Locate every blood parasite and identify its species.
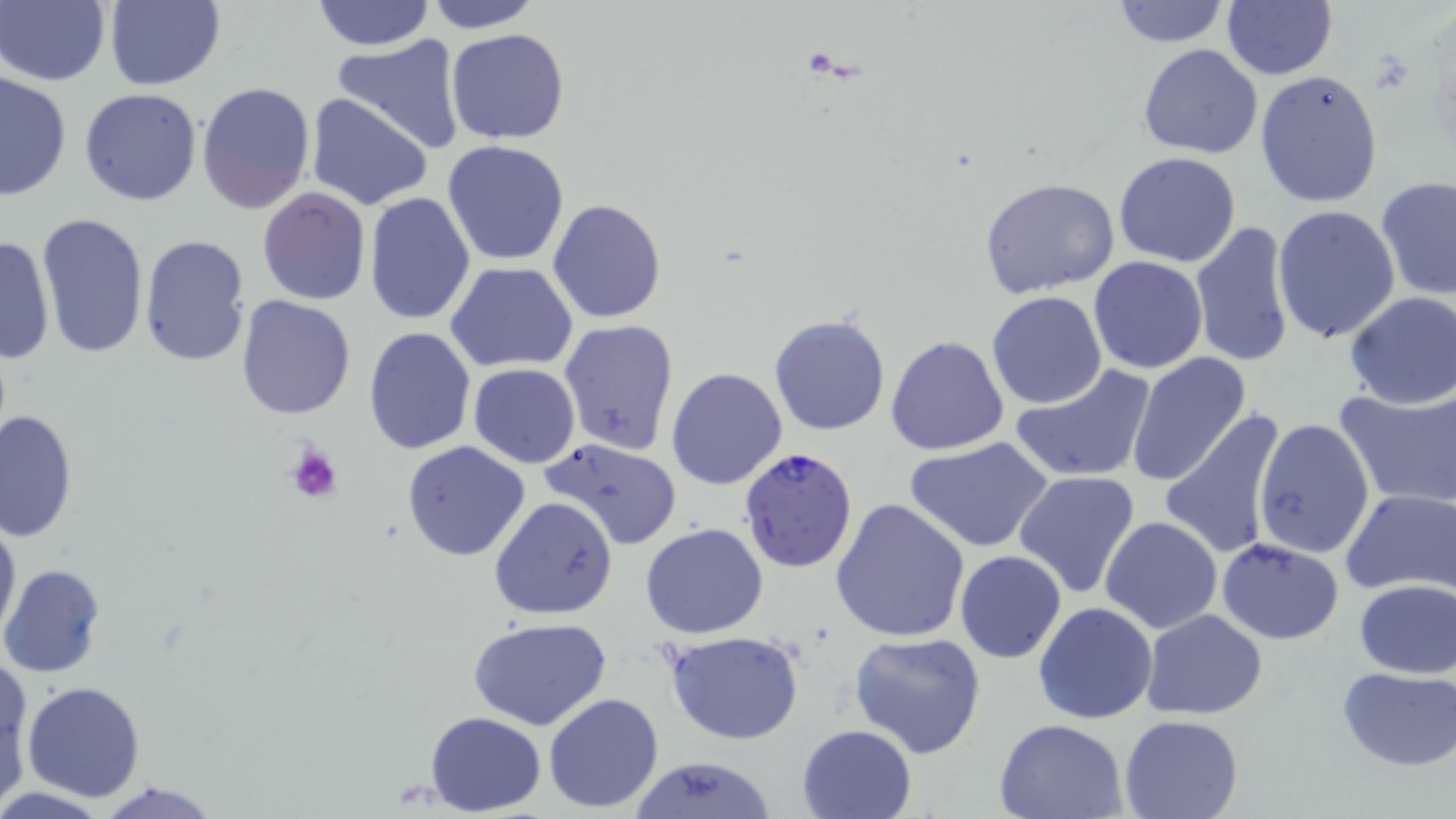
Approximate bounding boxes as (x1,y1)-(x2,y2) corner pairs in pixels.
Plasmodium falciparum-infected red blood cells: (737,446)-(860,576).
No Plasmodium ovale, Plasmodium malariae, Plasmodium vivax, Babesia divergens, or Trypanosoma brucei observed.

Platelet locations: (285,442)-(343,506). Uninfected red blood cell locations: (0,0)-(110,87), (310,0)-(434,52), (423,0)-(543,32), (1107,0)-(1230,49), (101,1)-(226,90), (1222,2)-(1337,79), (445,28)-(571,145), (332,37)-(466,156), (1137,44)-(1262,159), (1255,69)-(1384,212), (0,71)-(72,201), (197,81)-(316,217), (80,87)-(201,207), (304,92)-(435,211), (441,140)-(570,266), (1113,152)-(1242,268), (1376,176)-(1456,302), (978,177)-(1121,300), (257,187)-(372,307), (363,193)-(476,325), (548,198)-(666,323), (1273,205)-(1403,344), (35,213)-(152,364), (1189,220)-(1300,369), (0,234)-(54,367), (137,234)-(251,368), (1088,255)-(1209,375), (444,261)-(579,373), (987,291)-(1108,409), (1342,291)-(1456,410), (236,296)-(356,420), (769,314)-(892,437), (558,319)-(679,455), (362,327)-(477,455), (886,335)-(1010,456), (1126,353)-(1253,487), (467,363)-(580,469), (1012,364)-(1157,485), (666,367)-(788,491), (1334,382)-(1456,511), (1160,407)-(1288,560), (0,409)-(77,543), (1252,418)-(1376,560), (906,436)-(1055,554), (537,437)-(683,550), (401,441)-(532,562), (1013,470)-(1142,599), (1339,487)-(1454,598), (488,496)-(619,621), (830,498)-(969,643), (0,510)-(21,646), (1098,517)-(1224,636), (641,522)-(768,639), (1216,538)-(1345,644), (954,550)-(1068,664), (0,564)-(106,679), (1353,579)-(1455,677), (1032,601)-(1159,724), (1140,609)-(1268,719), (467,617)-(613,732), (664,630)-(807,745), (849,631)-(987,757), (505,645)-(659,791), (1,660)-(32,804), (1337,665)-(1454,769), (22,680)-(147,803), (543,692)-(665,814), (424,710)-(545,815), (1119,715)-(1244,819), (994,718)-(1132,818), (796,724)-(919,817), (627,756)-(779,818), (91,779)-(225,818). Slide-level diagnosis: Plasmodium falciparum. Light microscopy. 1000x magnification. Single field of view. May-Grünwald-Giemsa stain. Thin blood film. Image is 1456×819 pixels.